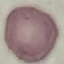

malaria status = uninfected
stain = Giemsa
preparation = thin blood smear
capture = smartphone camera at the microscope eyepiece
image type = cell patch, automatically extracted from a larger field of view and resized to 64 × 64 pixels